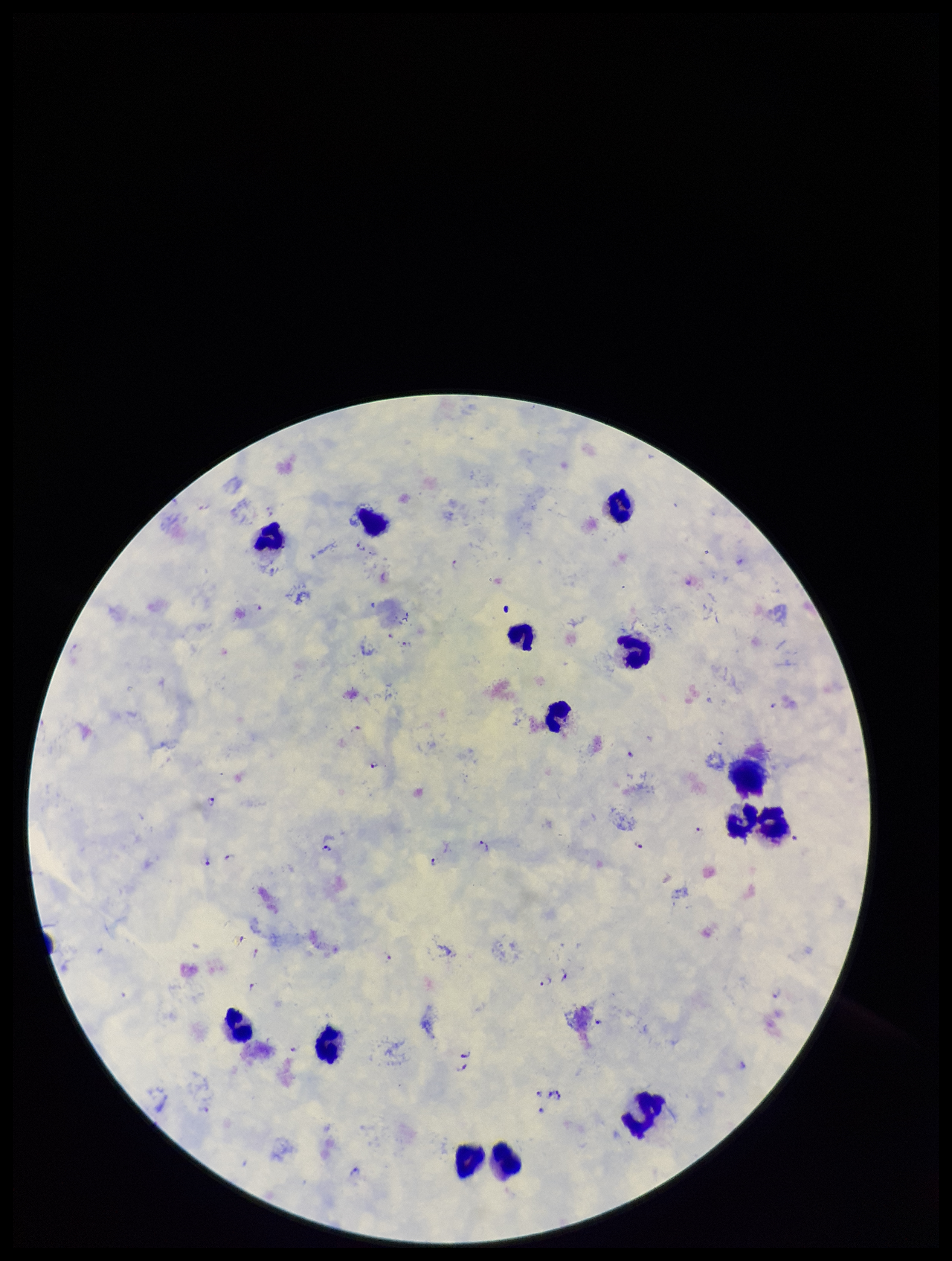
patient malaria status = positive
leukocyte count = 14
Plasmodium parasites = seen
capture = smartphone photograph through the microscope eyepiece
stain = Giemsa
field of view = one from this slide
parasite count = 33
species reported for this patient = Plasmodium falciparum
image size = 952×1261 pixels
preparation = thick